Assess this cell for malaria.
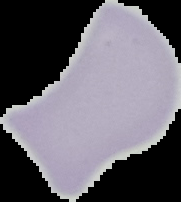

Uninfected.

From a thin blood film. The area outside the segmented cell region is set to black. Image is 181×202 pixels.